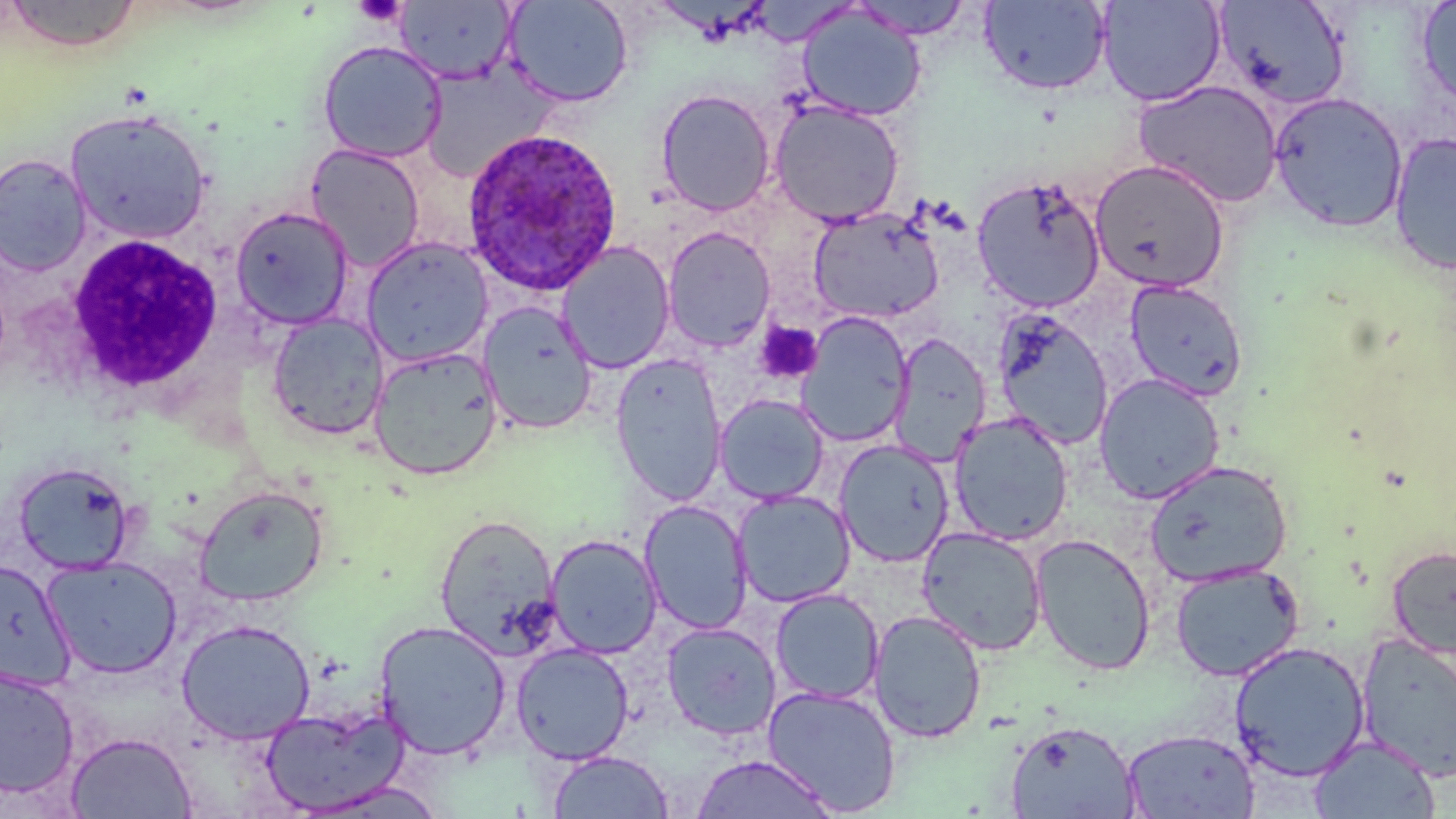

Approximate bounding boxes as [x1, y1, x2, y2] in pixels. Plasmodium ovale-infected red blood cell locations: [460, 128, 622, 297]. White blood cell locations: [65, 233, 225, 397]. Platelet locations: [353, 0, 408, 27], [755, 321, 822, 384]. Uninfected red blood cell locations: [3, 0, 142, 53], [394, 0, 517, 84], [502, 0, 634, 108], [850, 0, 974, 40], [1097, 0, 1226, 106], [978, 1, 1112, 96], [1213, 1, 1352, 112], [1416, 1, 1456, 112], [797, 5, 925, 122], [317, 40, 447, 163], [418, 61, 559, 182], [1133, 80, 1283, 208], [654, 88, 776, 216], [1269, 91, 1408, 233], [769, 100, 905, 227], [66, 109, 212, 245], [1388, 131, 1456, 276], [306, 143, 425, 272], [0, 153, 92, 276], [1090, 160, 1230, 293], [971, 175, 1107, 314], [229, 206, 354, 330], [808, 206, 944, 324], [662, 226, 776, 352], [360, 237, 494, 368], [556, 242, 676, 374], [1124, 279, 1248, 401], [478, 301, 598, 434], [991, 308, 1114, 450], [795, 311, 913, 449], [266, 313, 390, 441], [890, 333, 991, 464], [368, 346, 503, 481], [610, 355, 727, 507], [1094, 373, 1225, 504], [714, 394, 829, 505], [949, 412, 1074, 546], [833, 439, 955, 568], [1143, 460, 1293, 586], [12, 461, 136, 574], [194, 484, 329, 607], [733, 490, 856, 608], [639, 500, 753, 636], [434, 513, 562, 658], [917, 526, 1048, 656], [545, 534, 662, 659], [1030, 534, 1156, 675], [1386, 544, 1456, 657], [41, 555, 183, 679], [1, 557, 75, 692], [1169, 563, 1304, 682], [769, 589, 884, 705], [868, 609, 987, 744], [176, 619, 316, 745], [373, 619, 511, 760], [661, 622, 781, 741], [1356, 632, 1456, 782], [1229, 641, 1369, 780], [511, 642, 634, 765], [0, 667, 80, 800], [762, 685, 901, 815], [259, 702, 411, 816], [1004, 719, 1140, 819], [1121, 728, 1260, 818], [65, 731, 197, 818], [1309, 734, 1440, 818], [547, 750, 674, 818], [690, 753, 836, 818], [294, 780, 449, 818]. Slide-level diagnosis: Plasmodium ovale. Image is 1456×819 pixels. Thin blood film. Light microscopy. Single field of view. Captured at 1000x magnification. May-Grünwald-Giemsa stain.